Name the blood parasite species.
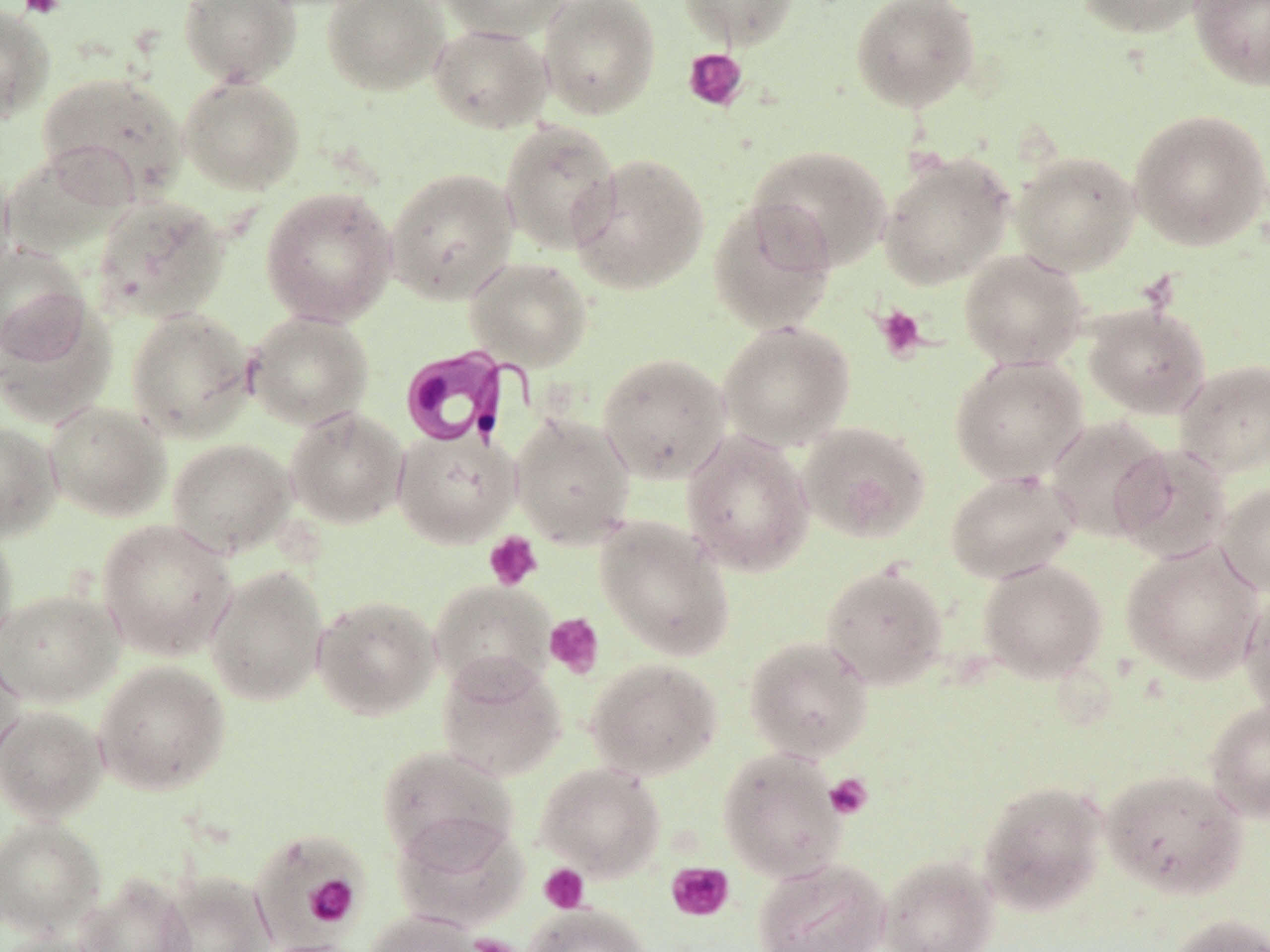

Trypanosoma brucei.

Summary:
  - Coordinate format: approximate bounding boxes as (x1, y1, x2, y2) in pixels
  - Trypanosoma brucei locations: (396, 343, 532, 449)
  - Platelet locations: (17, 0, 65, 19), (683, 48, 748, 111), (873, 304, 928, 362), (483, 531, 543, 591), (544, 613, 605, 678), (824, 773, 873, 820), (666, 861, 734, 922), (539, 863, 589, 913), (303, 874, 360, 927), (466, 934, 522, 952)
  - Uninfected red blood cell locations: (178, 0, 302, 87), (322, 0, 448, 95), (439, 0, 572, 41), (539, 0, 661, 119), (679, 0, 799, 49), (850, 0, 981, 112), (1076, 0, 1213, 39), (1189, 0, 1270, 90), (0, 3, 55, 124), (428, 23, 552, 133), (35, 70, 188, 205), (179, 75, 305, 194), (1129, 108, 1270, 252), (500, 120, 622, 255), (748, 145, 892, 272), (1, 148, 133, 257), (1010, 150, 1141, 276), (878, 152, 1014, 289), (570, 153, 710, 295), (0, 159, 16, 290), (386, 168, 518, 304), (260, 187, 397, 327), (92, 196, 230, 323), (707, 196, 838, 335), (0, 244, 89, 364), (959, 250, 1089, 369), (464, 257, 594, 371), (0, 297, 117, 428), (1083, 303, 1211, 419), (126, 308, 255, 442), (244, 311, 374, 430), (718, 321, 855, 450), (597, 352, 731, 483), (950, 355, 1089, 485), (1174, 359, 1270, 477), (44, 401, 171, 522), (285, 407, 408, 528), (510, 413, 635, 548), (1044, 416, 1172, 542), (0, 421, 62, 541), (797, 421, 931, 543), (392, 426, 519, 548), (681, 430, 814, 576), (167, 438, 296, 557), (1111, 444, 1233, 562), (944, 469, 1080, 583), (1217, 482, 1270, 595), (595, 517, 735, 662), (96, 519, 238, 660), (0, 526, 18, 655), (1121, 541, 1265, 683), (978, 558, 1107, 682), (820, 563, 949, 690), (205, 565, 329, 706), (430, 579, 556, 696), (1239, 586, 1270, 721), (0, 588, 124, 707), (312, 594, 441, 720), (744, 635, 873, 762), (0, 644, 27, 774), (437, 654, 567, 781), (585, 657, 723, 780), (93, 660, 231, 795), (1204, 701, 1270, 822), (0, 704, 108, 823), (376, 744, 518, 865), (718, 747, 848, 882), (536, 761, 665, 880), (1100, 767, 1248, 899), (977, 779, 1109, 915), (391, 813, 528, 933), (0, 817, 106, 937), (248, 829, 368, 946), (878, 855, 998, 951), (752, 858, 890, 951), (157, 871, 276, 952), (73, 873, 196, 952), (525, 903, 651, 952), (362, 910, 482, 952), (1165, 913, 1270, 952), (0, 931, 110, 952), (252, 938, 366, 952)
  - Magnification: 1000x
  - Field of view: single
  - Image size: 1270×952 pixels
  - Preparation: thin blood film
  - Modality: optical microscopy
  - Stain: May-Grünwald-Giemsa